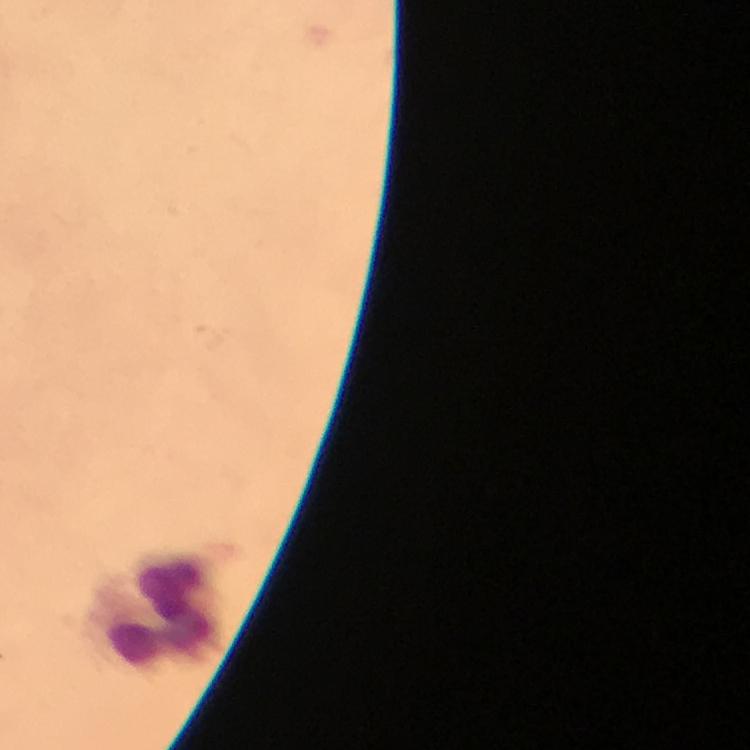
Approximate centers as (x, y) in pixels. Leukocyte locations: (156, 609). Photographed with a smartphone mounted on the microscope. From a diagnostic examination for malaria. Cropped region of a single field of view. Image is 750×750 pixels. 100x magnification. Plasmodium parasites: none detected. Giemsa-stained preparation. Thick blood smear. Immersion oil was used.